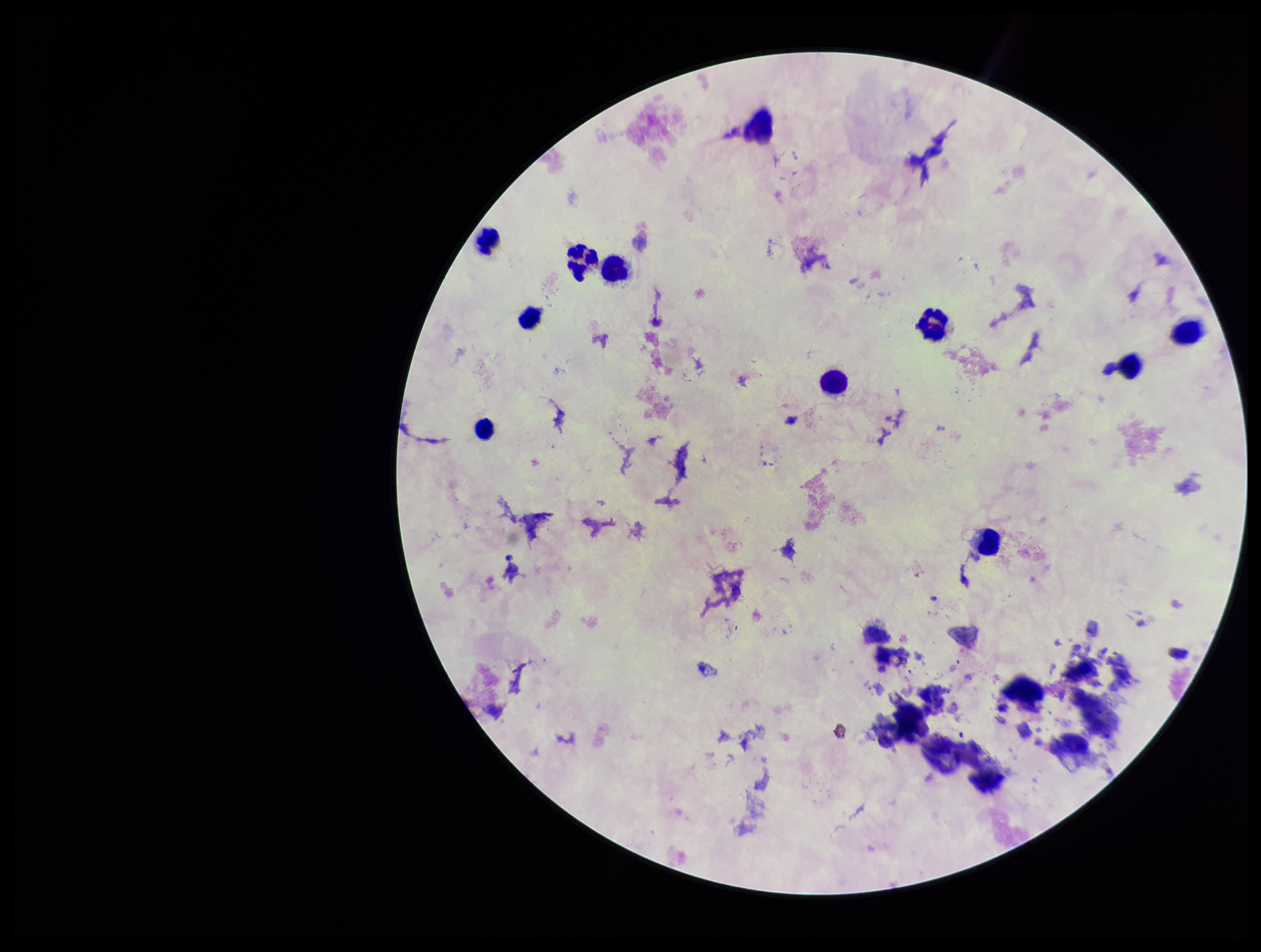 Smartphone photograph taken through the eyepiece of a microscope. Patient malaria status: negative. Stained with Giemsa. Leukocyte count: 10. Image is 1261×952 pixels. Parasite count: 0. Plasmodium parasites: none seen. Preparation: thick smear. One field from this slide.